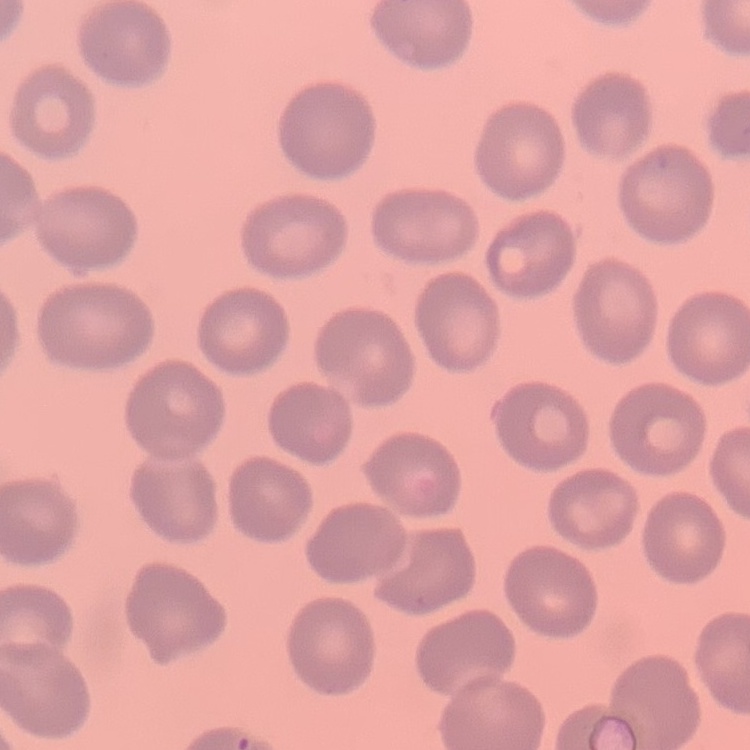

red blood cell morphology = no rouleaux formation
stain = Field's or Giemsa
preparation = thin peripheral smear
image type = square crop of a larger photomicrograph